Assess this cell for malaria.
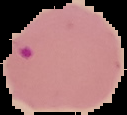
Parasitized.

From a thin blood film. Image is 127×115 pixels. The area outside the segmented cell region is set to black.